Locate platelets.
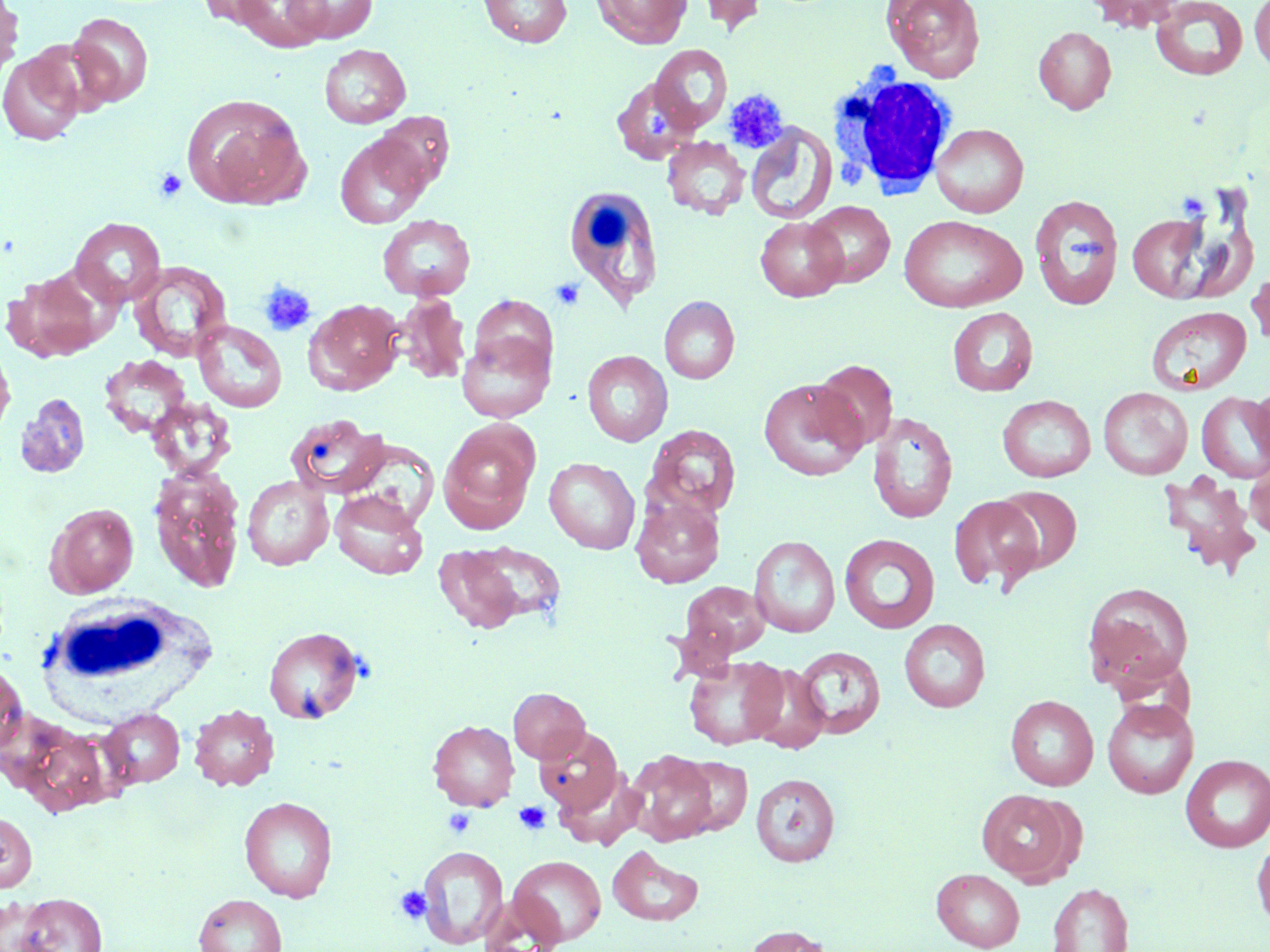
Approximate bounding boxes as (x1,y1)-(x2,y2) corner pairs in pixels.
Platelets: (723,89)-(788,153), (640,106)-(676,141), (154,168)-(187,202), (550,278)-(586,311), (257,280)-(317,337), (514,801)-(550,835), (443,808)-(476,838), (395,884)-(432,925).

slide_level_diagnosis: negative for blood parasites
white_blood_cell_locations: 'approximate bounding boxes as (x1,y1)-(x2,y2) corner pairs in pixels: (830,71)-(960,199), (559,183)-(662,307), (45,594)-(215,713)'
field_of_view: single
image_size: 1270×952 pixels
magnification: 1000x
preparation: thin blood film
modality: light microscopy
uninfected_red_blood_cell_locations: 'approximate bounding boxes as (x1,y1)-(x2,y2) corner pairs in pixels: (0,0)-(24,81), (197,0)-(277,27), (229,0)-(329,52), (283,0)-(378,44), (478,0)-(573,47), (593,0)-(691,48), (695,0)-(767,34), (882,0)-(986,82), (1086,0)-(1181,32), (1249,0)-(1270,72), (1150,1)-(1249,81), (68,12)-(153,108), (1034,26)-(1116,114), (319,44)-(411,128), (649,44)-(732,135), (0,49)-(85,145), (611,75)-(705,166), (181,93)-(311,210), (372,112)-(454,194), (930,123)-(1029,217), (746,124)-(836,225), (335,132)-(433,228), (662,137)-(750,219), (1029,194)-(1123,309), (805,201)-(895,287), (899,214)-(1026,312), (1127,214)-(1211,303), (377,215)-(476,301), (756,216)-(847,301), (70,218)-(166,307), (129,261)-(231,362), (1247,265)-(1270,352), (2,267)-(109,363), (393,294)-(471,385), (659,295)-(740,384), (305,299)-(404,394), (947,306)-(1038,397), (1146,306)-(1251,396), (193,320)-(287,413), (456,331)-(554,423), (0,341)-(15,442), (582,350)-(673,446), (99,355)-(193,440), (812,359)-(899,452), (758,379)-(867,481), (1252,380)-(1270,471), (1098,387)-(1193,479), (1197,391)-(1270,482), (15,392)-(91,480), (997,395)-(1096,482), (145,397)-(237,480), (867,411)-(958,524), (285,414)-(391,498), (439,422)-(539,531), (646,424)-(741,520), (1244,456)-(1270,541), (544,457)-(640,554), (148,467)-(246,593), (1157,472)-(1261,578), (242,476)-(333,570), (995,485)-(1082,574), (330,490)-(428,579), (948,495)-(1043,593), (631,498)-(724,587), (46,503)-(139,597), (839,533)-(940,634), (749,535)-(840,638), (467,540)-(568,626), (431,543)-(531,635), (677,580)-(770,664), (1082,583)-(1194,691), (899,619)-(990,712), (264,626)-(365,724), (794,646)-(886,739), (683,655)-(788,750), (0,661)-(27,757), (744,663)-(830,753), (508,687)-(590,763), (1005,695)-(1098,791), (1101,698)-(1198,799), (189,703)-(279,791), (99,708)-(184,789), (428,720)-(519,811), (534,725)-(623,816), (629,752)-(718,845), (1180,754)-(1270,853), (679,756)-(752,835), (555,770)-(646,849), (751,772)-(840,867), (976,789)-(1078,885), (239,796)-(338,902), (0,812)-(36,892), (1252,833)-(1270,929), (417,844)-(509,949), (608,845)-(704,927), (508,855)-(606,947), (932,867)-(1025,951), (1047,883)-(1134,951), (14,893)-(107,952), (194,894)-(287,952), (743,924)-(833,952)'
stain: May-Grünwald-Giemsa